Point out each Plasmodium parasite.
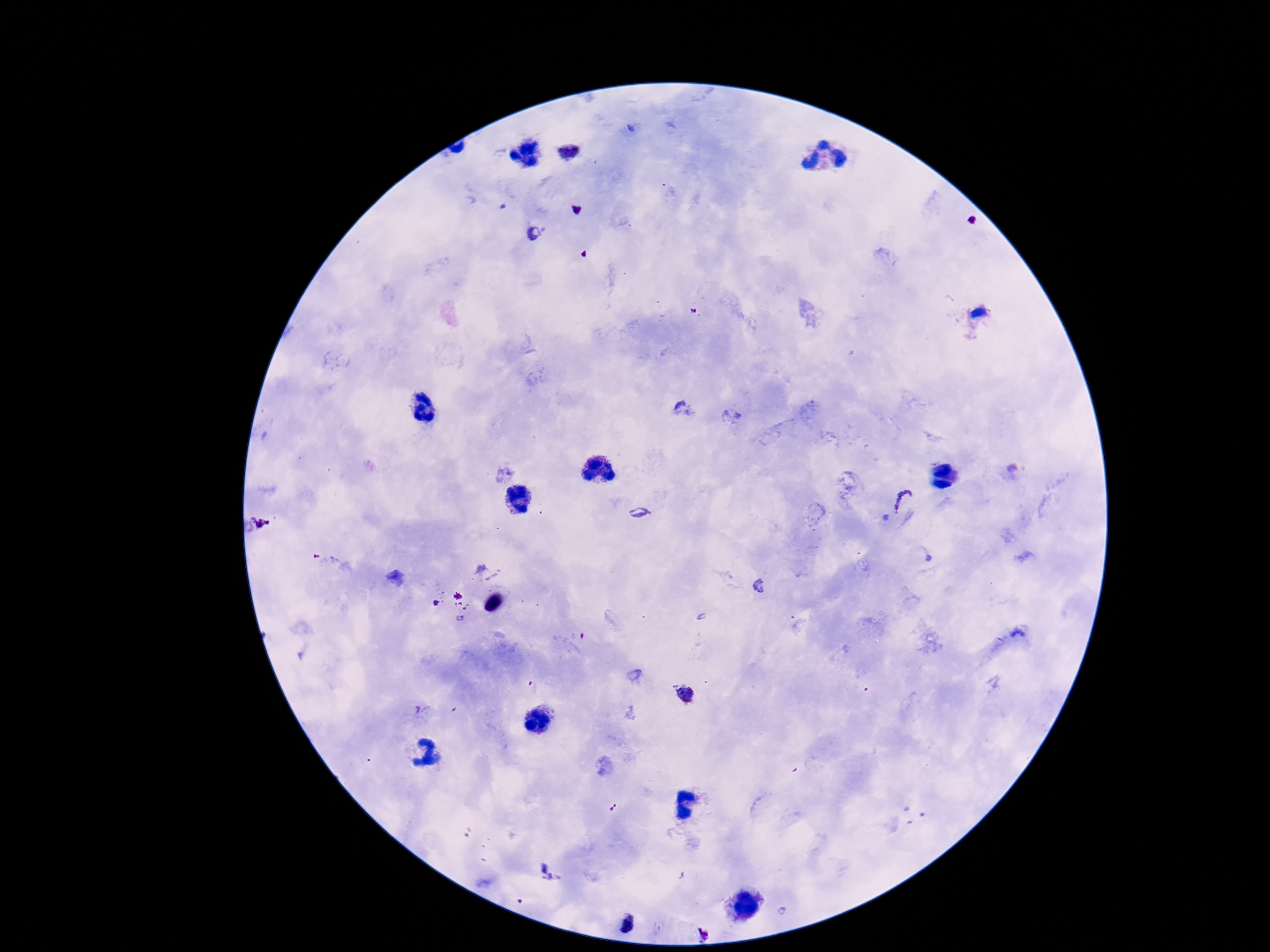
Approximate centers as (x, y) in pixels.
Plasmodium parasites: (567, 152), (541, 235), (683, 409), (902, 500), (640, 513), (683, 696), (549, 874), (626, 925).

Image is 1270×952 pixels. Giemsa-stained preparation. Thick blood film. 100x magnification. One field from this slide. Patient malaria status: infected. Smartphone photograph taken through the microscope eyepiece.